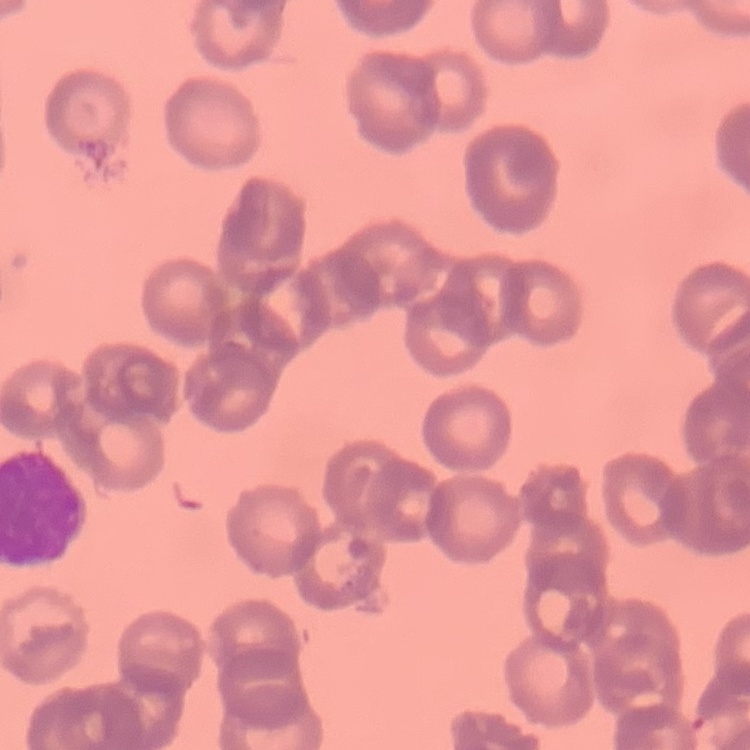

Summary:
  - Red blood cell morphology: rouleaux formation
  - Preparation: thin blood film
  - Stain: Field's or Giemsa
  - Image type: square crop of a larger photomicrograph